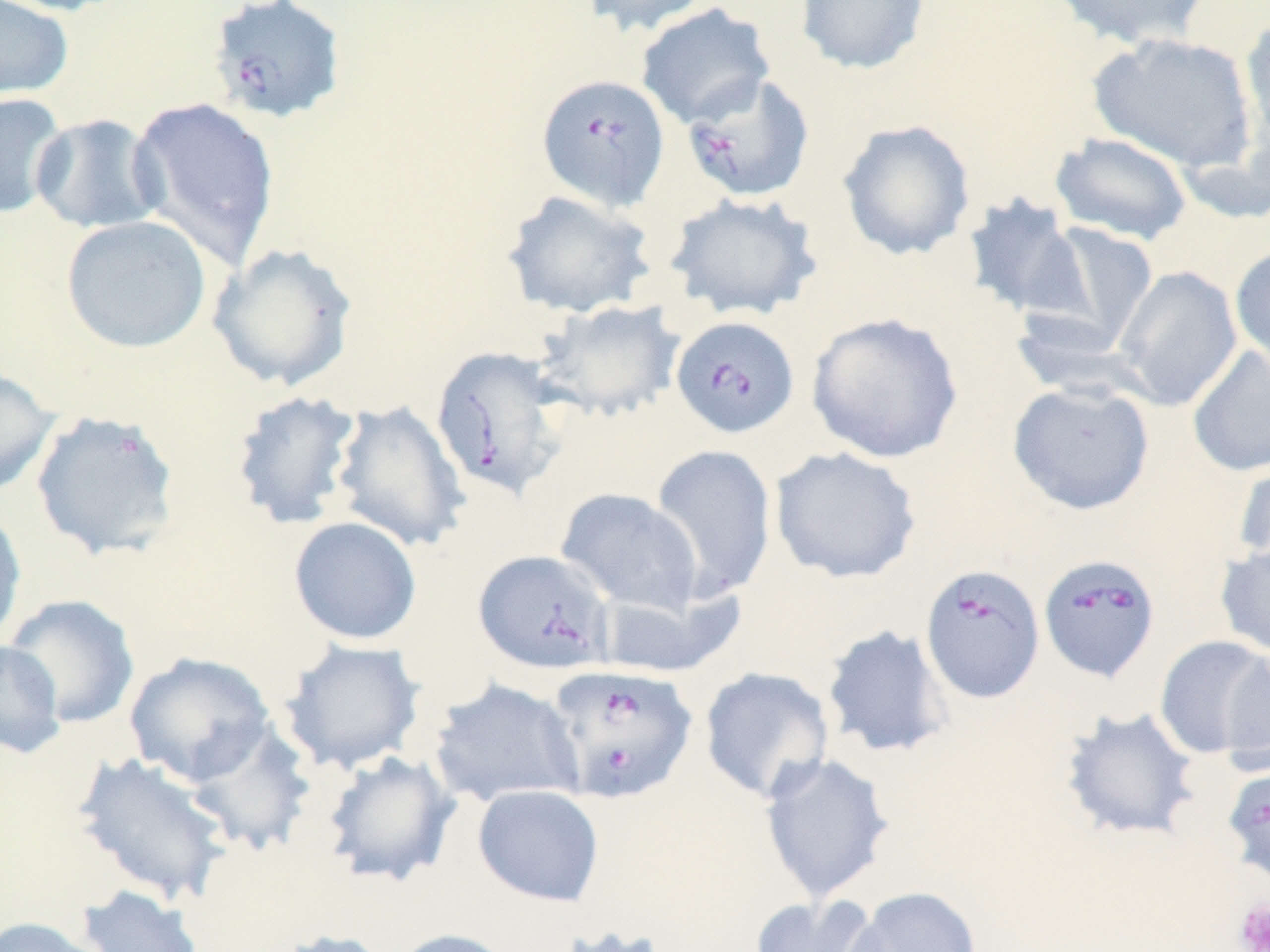
Summary:
  - Coordinate format: approximate bounding boxes as (x1, y1, x2, y2) in pixels
  - Babesia divergens-infected red blood cell locations: (206, 0, 347, 124), (681, 72, 815, 204), (536, 75, 671, 212), (669, 315, 800, 439), (430, 345, 570, 501), (473, 549, 615, 675), (1038, 553, 1161, 682), (919, 564, 1046, 703), (546, 663, 699, 803), (1222, 762, 1270, 889)
  - Uninfected red blood cell locations: (0, 0, 129, 17), (0, 0, 75, 102), (579, 0, 714, 37), (795, 0, 930, 76), (1048, 0, 1214, 51), (635, 2, 776, 130), (1239, 13, 1270, 160), (1089, 30, 1259, 174), (0, 92, 69, 219), (127, 96, 281, 270), (30, 113, 165, 235), (836, 119, 976, 262), (1049, 132, 1193, 245), (501, 189, 656, 319), (665, 192, 824, 321), (961, 193, 1089, 321), (60, 215, 212, 354), (1030, 221, 1160, 353), (207, 243, 359, 391), (1229, 243, 1270, 372), (1113, 265, 1242, 411), (533, 298, 686, 423), (806, 311, 965, 464), (1187, 345, 1270, 477), (0, 365, 61, 498), (1007, 380, 1155, 515), (229, 389, 365, 531), (329, 399, 471, 553), (30, 410, 181, 562), (649, 443, 778, 601), (769, 446, 923, 584), (1232, 455, 1270, 574), (555, 487, 703, 616), (0, 504, 27, 648), (288, 516, 422, 645), (1215, 539, 1270, 659), (595, 584, 745, 679), (4, 594, 140, 728), (821, 623, 955, 760), (1154, 635, 1270, 759), (279, 638, 427, 774), (0, 639, 67, 759), (1221, 648, 1270, 777), (123, 651, 275, 787), (699, 666, 834, 804), (428, 677, 585, 808), (1058, 706, 1202, 843), (183, 720, 318, 857), (319, 749, 461, 888), (71, 750, 236, 907), (758, 752, 896, 904), (472, 784, 605, 907), (76, 884, 205, 952), (842, 886, 982, 952), (749, 893, 886, 952), (0, 916, 108, 952), (552, 923, 672, 952), (264, 928, 396, 952), (388, 928, 519, 952)
  - Platelet locations: (1234, 898, 1270, 952)
  - Slide-level diagnosis: Babesia divergens
  - Stain: May-Grünwald-Giemsa
  - Preparation: thin blood smear
  - Magnification: 1000x
  - Modality: light microscopy
  - Field of view: one of a larger specimen
  - Image size: 1270×952 pixels